Describe the morphology of the red blood cells.
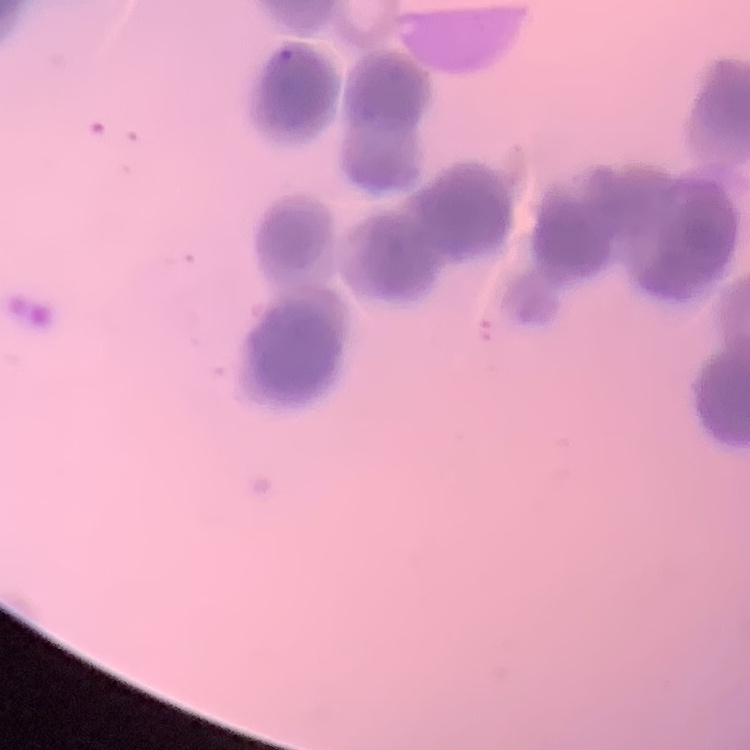
Rouleaux formation.

Summary:
  - Image type: square crop of a larger photomicrograph
  - Stain: Field's or Giemsa
  - Preparation: thin blood smear